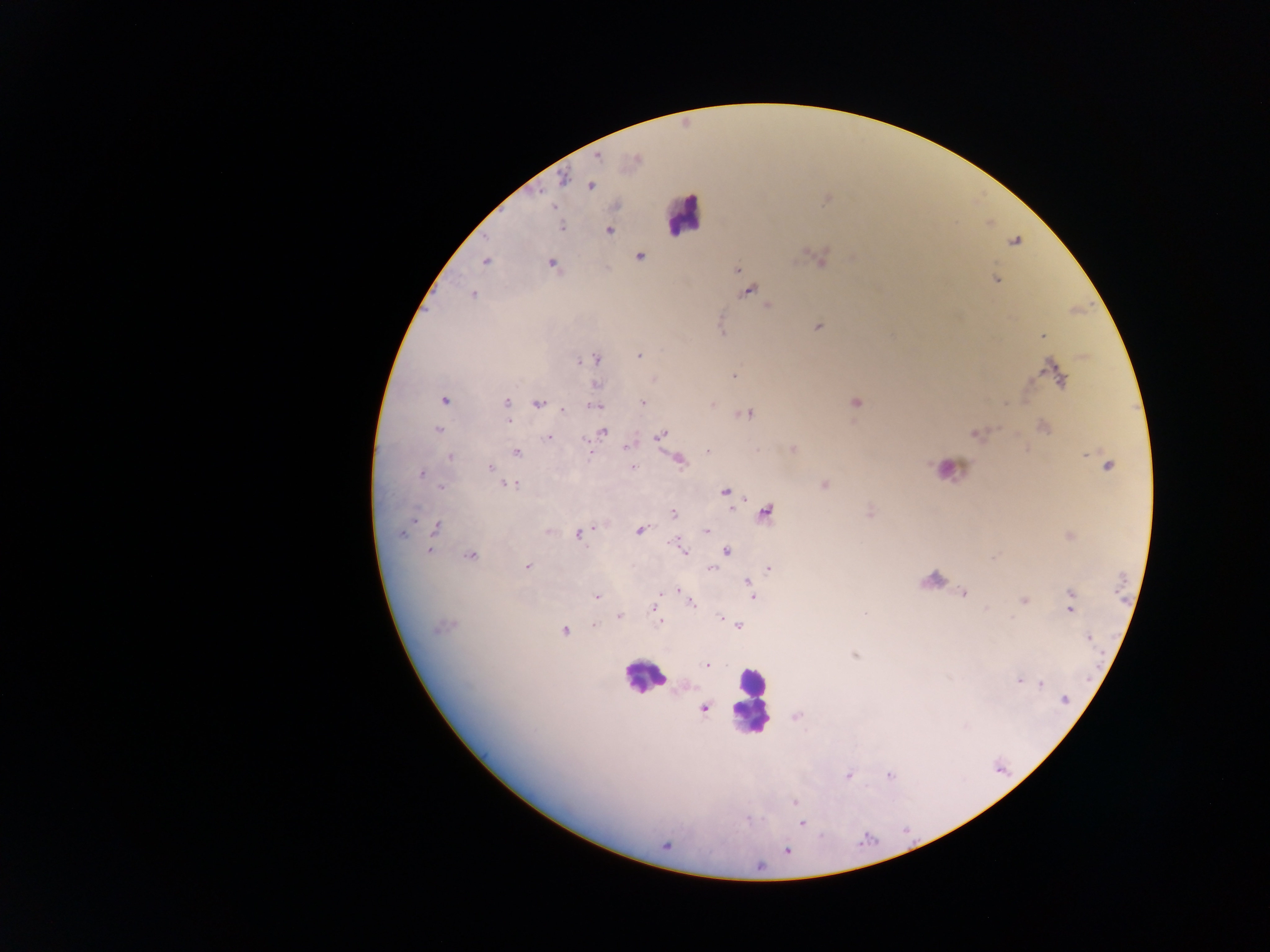

Approximate centers as {x, y} in pixels.
Summary:
  - Plasmodium parasite locations: {597, 157}, {633, 161}, {563, 179}, {588, 185}, {589, 185}, {826, 199}, {561, 227}, {608, 230}, {1015, 241}, {639, 256}, {819, 257}, {855, 258}, {486, 260}, {551, 264}, {736, 269}, {995, 279}, {746, 290}, {472, 294}, {768, 306}, {819, 326}, {1043, 336}, {639, 354}, {595, 359}, {579, 361}, {733, 375}, {1056, 376}, {655, 379}, {594, 383}, {444, 400}, {505, 402}, {642, 402}, {854, 402}, {538, 403}, {712, 404}, {594, 406}, {747, 413}, {1043, 426}, {438, 430}, {602, 432}, {975, 433}, {660, 436}, {549, 438}, {590, 449}, {791, 449}, {707, 451}, {516, 452}, {1085, 452}, {449, 456}, {678, 459}, {1107, 464}, {633, 466}, {490, 467}, {421, 473}, {508, 484}, {823, 484}, {441, 487}, {724, 491}, {765, 511}, {869, 511}, {673, 514}, {413, 518}, {436, 527}, {639, 530}, {548, 531}, {706, 531}, {401, 532}, {577, 533}, {1068, 535}, {676, 543}, {682, 548}, {429, 550}, {726, 551}, {470, 555}, {993, 557}, {527, 565}, {711, 567}, {768, 568}, {748, 582}, {751, 590}, {678, 591}, {964, 593}, {597, 596}, {752, 597}, {1024, 600}, {691, 603}, {654, 607}, {1070, 607}, {865, 614}, {619, 615}, {658, 616}, {719, 616}, {660, 622}, {594, 624}, {738, 625}, {443, 627}, {564, 630}, {1088, 638}, {853, 655}, {707, 664}, {1018, 679}, {1041, 684}, {1064, 700}, {702, 707}, {796, 716}, {847, 775}, {889, 775}, {795, 803}, {801, 822}, {665, 844}, {786, 850}
  - Leukocyte locations: {684, 214}, {948, 470}, {933, 582}, {644, 676}, {750, 703}
  - Image size: 1270×952 pixels
  - Field of view: single
  - Country: Ghana
  - Preparation: thick blood smear
  - Capture: mobile-phone photograph through a microscope